Describe the morphology of the red blood cells.
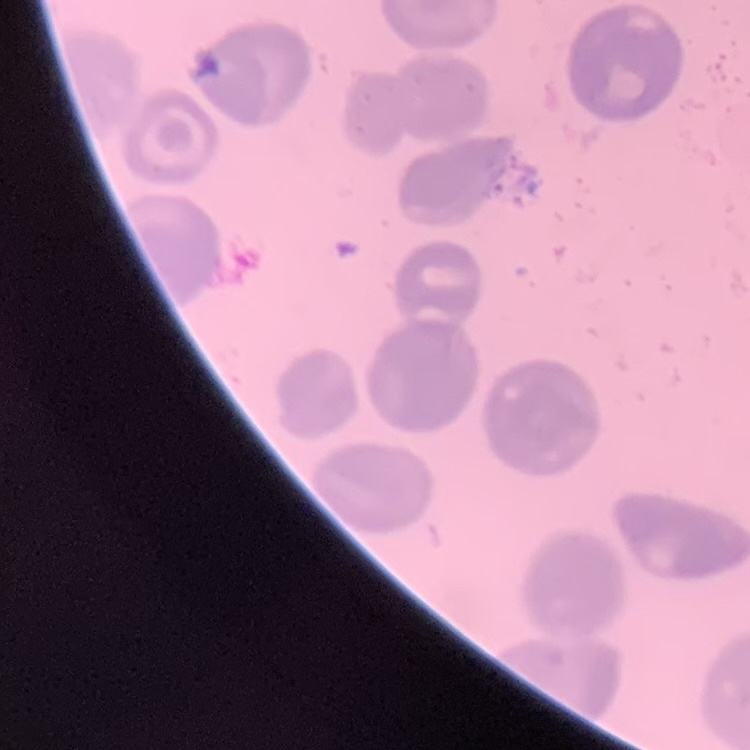
No rouleaux formation.

Summary:
  - Preparation: thin blood smear
  - Stain: Field's or Giemsa
  - Image type: one tile cut from a larger photomicrograph